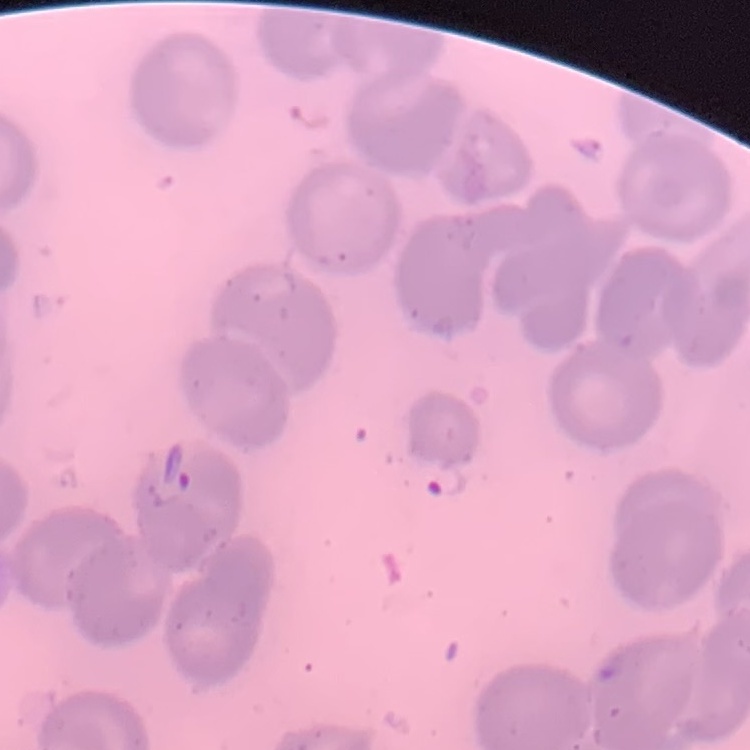 The erythrocytes exhibit no rouleaux formation. Thin blood smear. Stained with either Field's or Giemsa. Square crop of a larger photomicrograph.